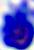
{
  "magnification": "400x",
  "modality": "micrograph",
  "identification": "white blood cell"
}